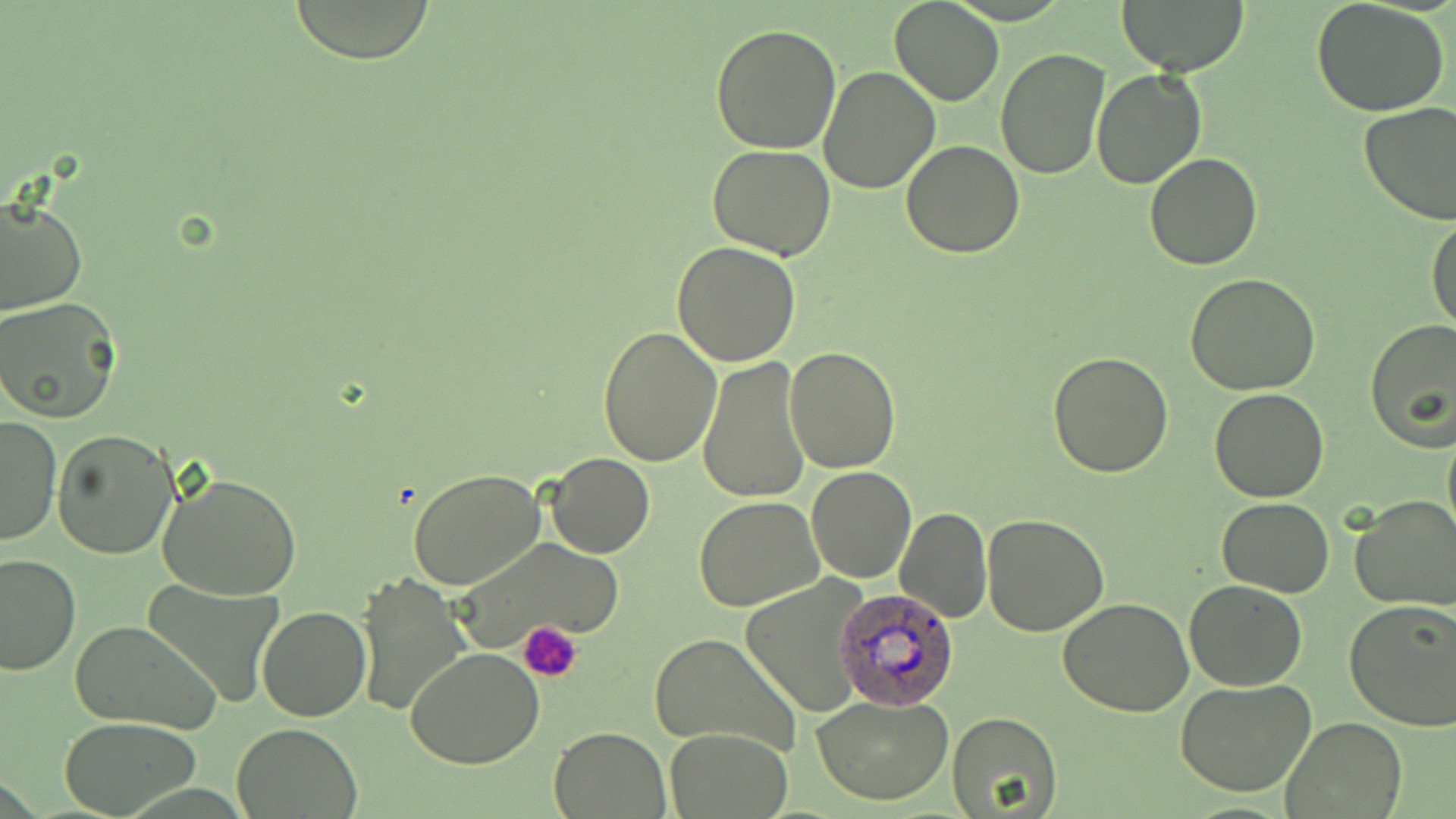

Summary:
  - Coordinate format: approximate bounding boxes as named x1/y1/x2/y2 corners in pixels
  - Platelet locations: (x1=518, y1=622, x2=582, y2=682)
  - Uninfected red blood cell locations: (x1=289, y1=0, x2=435, y2=64), (x1=889, y1=0, x2=1004, y2=106), (x1=1116, y1=0, x2=1249, y2=74), (x1=1311, y1=1, x2=1452, y2=117), (x1=710, y1=23, x2=841, y2=155), (x1=994, y1=48, x2=1109, y2=179), (x1=818, y1=65, x2=940, y2=194), (x1=1092, y1=69, x2=1208, y2=189), (x1=1358, y1=101, x2=1456, y2=224), (x1=902, y1=139, x2=1024, y2=257), (x1=707, y1=145, x2=838, y2=259), (x1=1144, y1=152, x2=1263, y2=270), (x1=0, y1=195, x2=85, y2=316), (x1=1426, y1=213, x2=1456, y2=333), (x1=673, y1=242, x2=802, y2=367), (x1=1186, y1=273, x2=1320, y2=393), (x1=0, y1=298, x2=123, y2=422), (x1=1365, y1=320, x2=1455, y2=448), (x1=598, y1=327, x2=723, y2=465), (x1=785, y1=346, x2=900, y2=471), (x1=1048, y1=350, x2=1175, y2=478), (x1=697, y1=357, x2=811, y2=504), (x1=1209, y1=388, x2=1330, y2=503), (x1=0, y1=415, x2=60, y2=546), (x1=1442, y1=420, x2=1456, y2=544), (x1=53, y1=429, x2=180, y2=558), (x1=547, y1=452, x2=655, y2=558), (x1=807, y1=466, x2=916, y2=582), (x1=407, y1=468, x2=548, y2=591), (x1=158, y1=469, x2=302, y2=601), (x1=695, y1=495, x2=822, y2=611), (x1=1350, y1=496, x2=1456, y2=611), (x1=1215, y1=498, x2=1335, y2=596), (x1=894, y1=505, x2=991, y2=622), (x1=983, y1=515, x2=1110, y2=635), (x1=448, y1=537, x2=628, y2=654), (x1=0, y1=552, x2=79, y2=677), (x1=353, y1=574, x2=470, y2=713), (x1=738, y1=576, x2=874, y2=719), (x1=1184, y1=579, x2=1307, y2=691), (x1=138, y1=580, x2=284, y2=710), (x1=1058, y1=600, x2=1192, y2=717), (x1=1343, y1=600, x2=1456, y2=731), (x1=258, y1=606, x2=371, y2=722), (x1=69, y1=619, x2=222, y2=735), (x1=648, y1=633, x2=800, y2=756), (x1=406, y1=647, x2=546, y2=769), (x1=1175, y1=679, x2=1319, y2=799), (x1=813, y1=694, x2=956, y2=805), (x1=947, y1=709, x2=1062, y2=817), (x1=1281, y1=716, x2=1408, y2=819), (x1=60, y1=717, x2=202, y2=816), (x1=231, y1=723, x2=362, y2=817), (x1=549, y1=727, x2=669, y2=818), (x1=667, y1=727, x2=792, y2=819)
  - Plasmodium ovale-infected red blood cell locations: (x1=834, y1=587, x2=959, y2=710)
  - Slide-level diagnosis: Plasmodium ovale
  - Image size: 1456×819 pixels
  - Field of view: one of a larger specimen
  - Magnification: 1000x
  - Stain: May-Grünwald-Giemsa
  - Modality: light microscopy
  - Preparation: thin blood film